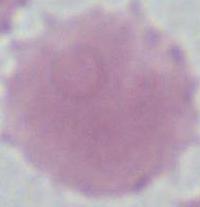 An erythrocyte is seen. Photomicrograph. 1000x magnification.